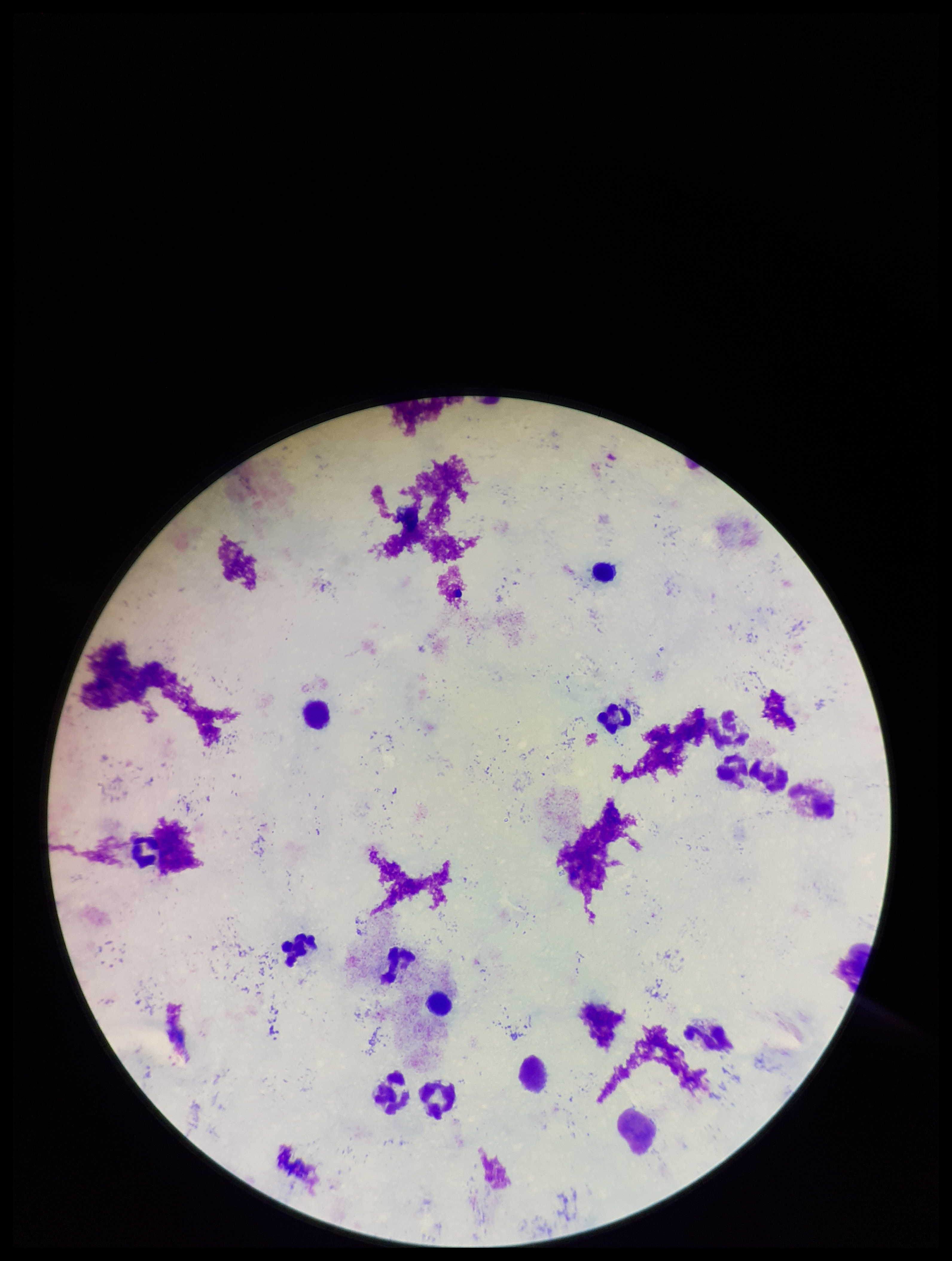
Summary:
  - Leukocyte count: 9
  - Image size: 952×1261 pixels
  - Plasmodium parasites: none detected
  - Capture: smartphone photograph through the microscope eyepiece
  - Stain: Giemsa
  - Parasite count: 0
  - Patient malaria status: negative
  - Field of view: one from this slide
  - Preparation: thick blood smear